Report the malaria status of this cell.
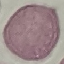

Uninfected.

capture = smartphone through the microscope eyepiece
preparation = thin blood smear
stain = Giemsa
image type = cell patch, automatically extracted from a larger field of view and resized to 64 × 64 pixels